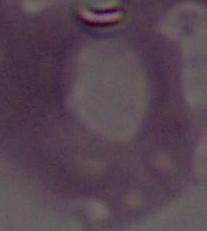

Summary:
  - Identification: erythrocyte
  - Modality: photomicrograph
  - Magnification: 1000x